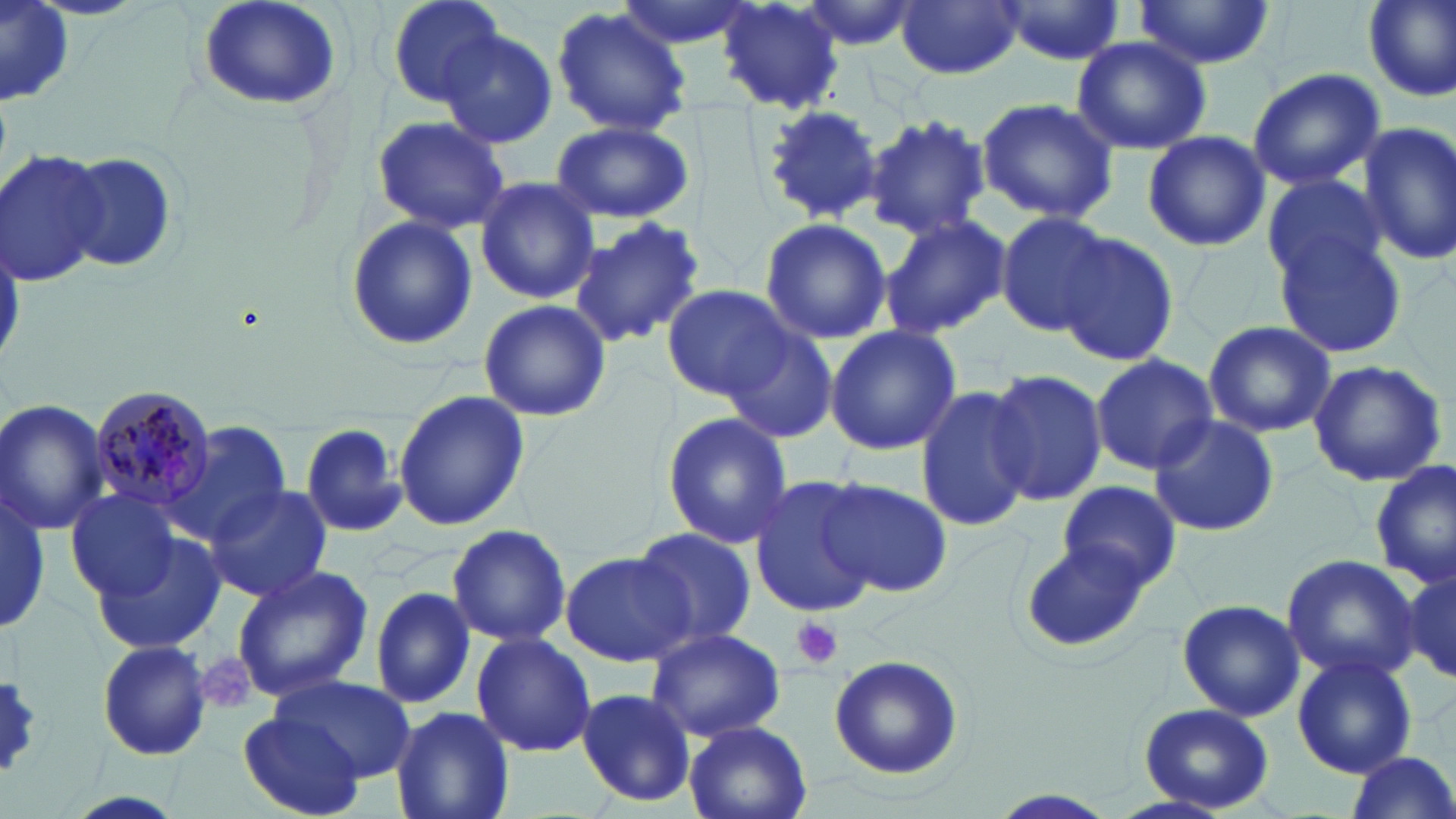

Approximate bounding boxes as named x1/y1/x2/y2 corners in pixels. Platelet locations: (x1=790, y1=616, x2=844, y2=669), (x1=194, y1=653, x2=258, y2=715). Uninfected red blood cell locations: (x1=385, y1=0, x2=509, y2=111), (x1=612, y1=0, x2=757, y2=50), (x1=794, y1=0, x2=923, y2=51), (x1=998, y1=0, x2=1124, y2=66), (x1=1134, y1=0, x2=1279, y2=71), (x1=1360, y1=0, x2=1456, y2=103), (x1=0, y1=2, x2=75, y2=105), (x1=195, y1=2, x2=340, y2=114), (x1=714, y1=2, x2=845, y2=112), (x1=896, y1=2, x2=1025, y2=79), (x1=551, y1=6, x2=694, y2=136), (x1=438, y1=28, x2=556, y2=149), (x1=1069, y1=36, x2=1211, y2=156), (x1=1246, y1=67, x2=1387, y2=190), (x1=976, y1=94, x2=1120, y2=223), (x1=761, y1=104, x2=881, y2=223), (x1=865, y1=113, x2=993, y2=242), (x1=370, y1=115, x2=512, y2=235), (x1=550, y1=120, x2=693, y2=224), (x1=1357, y1=123, x2=1456, y2=268), (x1=1140, y1=129, x2=1273, y2=252), (x1=2, y1=148, x2=111, y2=288), (x1=61, y1=151, x2=180, y2=275), (x1=474, y1=175, x2=599, y2=305), (x1=1260, y1=176, x2=1391, y2=289), (x1=994, y1=210, x2=1114, y2=336), (x1=877, y1=212, x2=1012, y2=341), (x1=343, y1=214, x2=478, y2=353), (x1=571, y1=216, x2=706, y2=348), (x1=758, y1=216, x2=891, y2=345), (x1=1056, y1=232, x2=1179, y2=369), (x1=1276, y1=235, x2=1408, y2=358), (x1=659, y1=284, x2=792, y2=398), (x1=478, y1=299, x2=612, y2=424), (x1=1202, y1=319, x2=1337, y2=439), (x1=824, y1=325, x2=961, y2=456), (x1=717, y1=326, x2=839, y2=442), (x1=1090, y1=354, x2=1218, y2=475), (x1=1307, y1=357, x2=1447, y2=488), (x1=983, y1=368, x2=1107, y2=505), (x1=913, y1=385, x2=1032, y2=530), (x1=394, y1=389, x2=528, y2=534), (x1=0, y1=398, x2=111, y2=538), (x1=659, y1=411, x2=794, y2=549), (x1=1147, y1=414, x2=1280, y2=537), (x1=168, y1=422, x2=291, y2=544), (x1=290, y1=422, x2=408, y2=539), (x1=1366, y1=460, x2=1456, y2=592), (x1=750, y1=475, x2=879, y2=618), (x1=821, y1=478, x2=952, y2=598), (x1=1058, y1=481, x2=1181, y2=593), (x1=203, y1=483, x2=333, y2=603), (x1=1322, y1=487, x2=1427, y2=656), (x1=64, y1=489, x2=187, y2=602), (x1=1, y1=493, x2=49, y2=633), (x1=443, y1=523, x2=573, y2=646), (x1=631, y1=526, x2=759, y2=647), (x1=90, y1=529, x2=228, y2=658), (x1=1019, y1=542, x2=1149, y2=655), (x1=559, y1=551, x2=694, y2=667), (x1=1282, y1=554, x2=1421, y2=683), (x1=1403, y1=562, x2=1456, y2=686), (x1=229, y1=565, x2=374, y2=702), (x1=369, y1=586, x2=476, y2=710), (x1=1176, y1=598, x2=1306, y2=722), (x1=646, y1=627, x2=786, y2=741), (x1=470, y1=631, x2=596, y2=758), (x1=95, y1=640, x2=214, y2=760), (x1=827, y1=653, x2=965, y2=779), (x1=1291, y1=653, x2=1417, y2=778), (x1=0, y1=672, x2=46, y2=780), (x1=272, y1=673, x2=416, y2=779), (x1=575, y1=688, x2=697, y2=805), (x1=1137, y1=703, x2=1275, y2=814), (x1=390, y1=706, x2=516, y2=819), (x1=238, y1=713, x2=366, y2=818), (x1=684, y1=720, x2=813, y2=819), (x1=1343, y1=753, x2=1456, y2=819), (x1=53, y1=789, x2=194, y2=819). Plasmodium malariae-infected red blood cell locations: (x1=86, y1=383, x2=219, y2=515). Slide-level diagnosis: Plasmodium malariae. Light microscopy. 1000x magnification. One field of a larger specimen. Thin blood smear. Image is 1456×819 pixels. May-Grünwald-Giemsa-stained preparation.